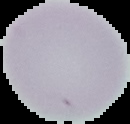

preparation = thin blood smear
image type = segmented cell region with the area outside set to black
image size = 130×124 pixels
result = negative for Plasmodium parasites